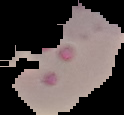

Summary:
  - Preparation: thin blood smear
  - Image size: 124×115 pixels
  - Image type: segmented cell region with the area outside set to black
  - Result: malaria parasites detected